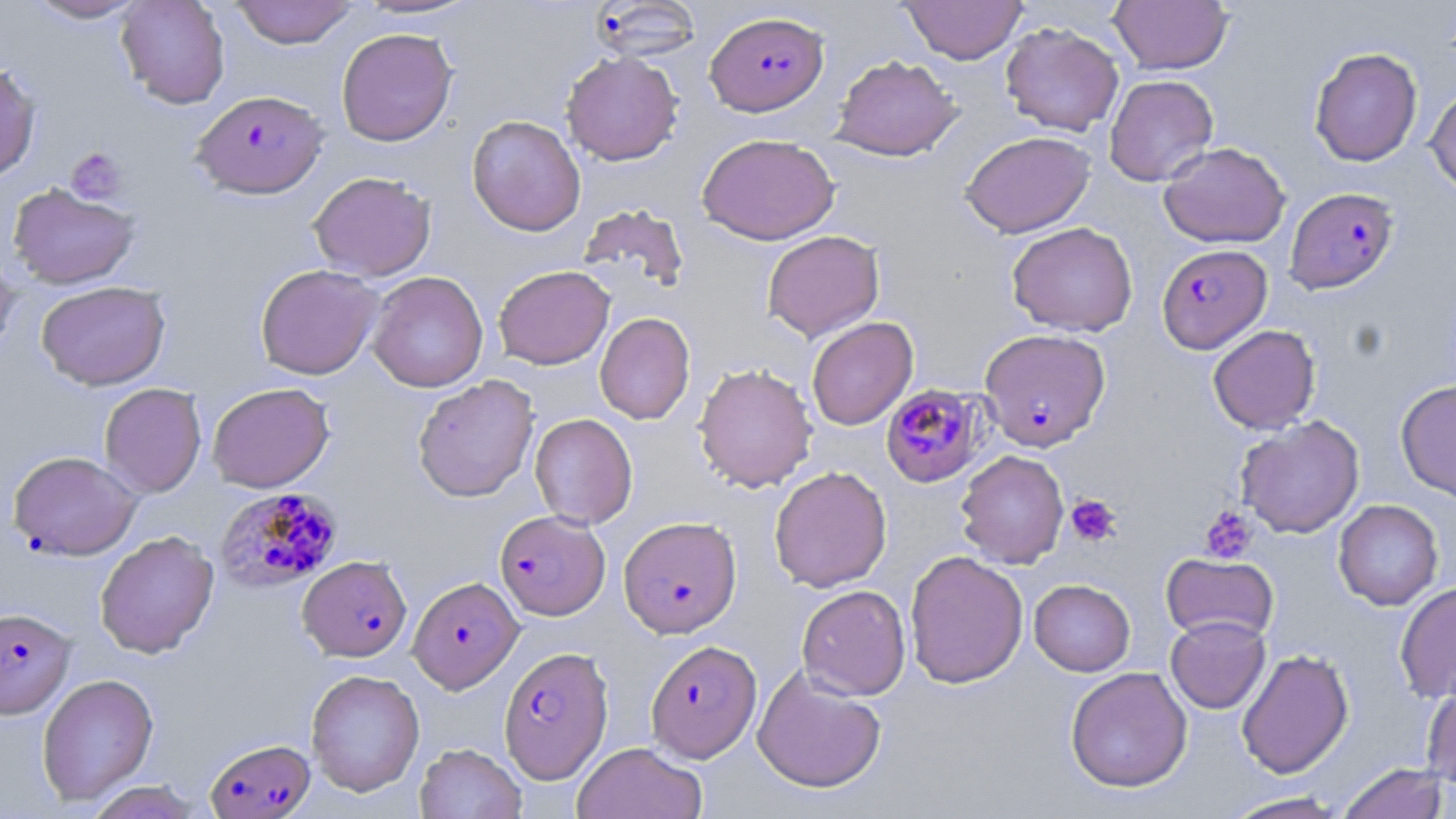
Approximate bounding boxes as named x1/y1/x2/y2 corners in pixels. Plasmodium falciparum-infected red blood cell locations: (x1=590, y1=1, x2=703, y2=62), (x1=705, y1=10, x2=828, y2=116), (x1=192, y1=90, x2=327, y2=198), (x1=1284, y1=187, x2=1399, y2=294), (x1=1157, y1=244, x2=1272, y2=354), (x1=979, y1=328, x2=1112, y2=451), (x1=879, y1=383, x2=988, y2=489), (x1=8, y1=450, x2=142, y2=560), (x1=214, y1=486, x2=343, y2=593), (x1=495, y1=510, x2=610, y2=620), (x1=618, y1=515, x2=742, y2=638), (x1=298, y1=555, x2=412, y2=661), (x1=408, y1=576, x2=523, y2=692), (x1=0, y1=607, x2=75, y2=718), (x1=645, y1=639, x2=762, y2=762), (x1=499, y1=646, x2=614, y2=783), (x1=205, y1=738, x2=315, y2=818). Uninfected red blood cell locations: (x1=24, y1=0, x2=150, y2=24), (x1=116, y1=0, x2=230, y2=109), (x1=230, y1=0, x2=359, y2=48), (x1=350, y1=0, x2=484, y2=21), (x1=899, y1=0, x2=1027, y2=64), (x1=1108, y1=0, x2=1233, y2=75), (x1=1000, y1=22, x2=1124, y2=136), (x1=336, y1=27, x2=457, y2=146), (x1=1309, y1=47, x2=1422, y2=167), (x1=561, y1=51, x2=683, y2=166), (x1=831, y1=55, x2=963, y2=161), (x1=0, y1=61, x2=41, y2=182), (x1=1104, y1=74, x2=1218, y2=186), (x1=1425, y1=84, x2=1456, y2=196), (x1=466, y1=115, x2=586, y2=236), (x1=960, y1=131, x2=1095, y2=238), (x1=697, y1=133, x2=839, y2=245), (x1=1158, y1=142, x2=1291, y2=248), (x1=308, y1=171, x2=436, y2=281), (x1=7, y1=183, x2=140, y2=289), (x1=578, y1=204, x2=690, y2=293), (x1=1006, y1=221, x2=1138, y2=337), (x1=762, y1=230, x2=885, y2=342), (x1=0, y1=248, x2=20, y2=360), (x1=255, y1=263, x2=383, y2=380), (x1=493, y1=265, x2=614, y2=369), (x1=367, y1=271, x2=488, y2=392), (x1=36, y1=280, x2=171, y2=390), (x1=594, y1=312, x2=695, y2=425), (x1=806, y1=316, x2=919, y2=430), (x1=1207, y1=325, x2=1321, y2=434), (x1=693, y1=362, x2=818, y2=493), (x1=413, y1=375, x2=539, y2=502), (x1=1396, y1=379, x2=1456, y2=503), (x1=207, y1=382, x2=334, y2=492), (x1=99, y1=383, x2=207, y2=498), (x1=529, y1=412, x2=638, y2=529), (x1=1235, y1=415, x2=1365, y2=538), (x1=955, y1=450, x2=1069, y2=568), (x1=769, y1=465, x2=892, y2=592), (x1=1333, y1=499, x2=1444, y2=611), (x1=95, y1=530, x2=219, y2=658), (x1=904, y1=550, x2=1029, y2=689), (x1=1161, y1=553, x2=1278, y2=644), (x1=1029, y1=579, x2=1135, y2=676), (x1=1394, y1=580, x2=1456, y2=704), (x1=797, y1=584, x2=910, y2=700), (x1=1166, y1=615, x2=1271, y2=714), (x1=1236, y1=648, x2=1354, y2=779), (x1=752, y1=666, x2=886, y2=794), (x1=1065, y1=666, x2=1192, y2=793), (x1=306, y1=668, x2=425, y2=796), (x1=36, y1=673, x2=159, y2=806), (x1=1421, y1=678, x2=1456, y2=789), (x1=414, y1=742, x2=526, y2=819), (x1=572, y1=742, x2=707, y2=819), (x1=1336, y1=762, x2=1450, y2=819), (x1=85, y1=781, x2=204, y2=819), (x1=1218, y1=792, x2=1352, y2=818). Platelet locations: (x1=65, y1=147, x2=127, y2=204), (x1=1065, y1=493, x2=1121, y2=547), (x1=1199, y1=505, x2=1258, y2=564). Slide-level diagnosis: Plasmodium falciparum. May-Grünwald-Giemsa stain. One field of a larger specimen. 1000x magnification. Image is 1456×819 pixels. Optical microscopy. Thin blood film.